Point out each leukocyte.
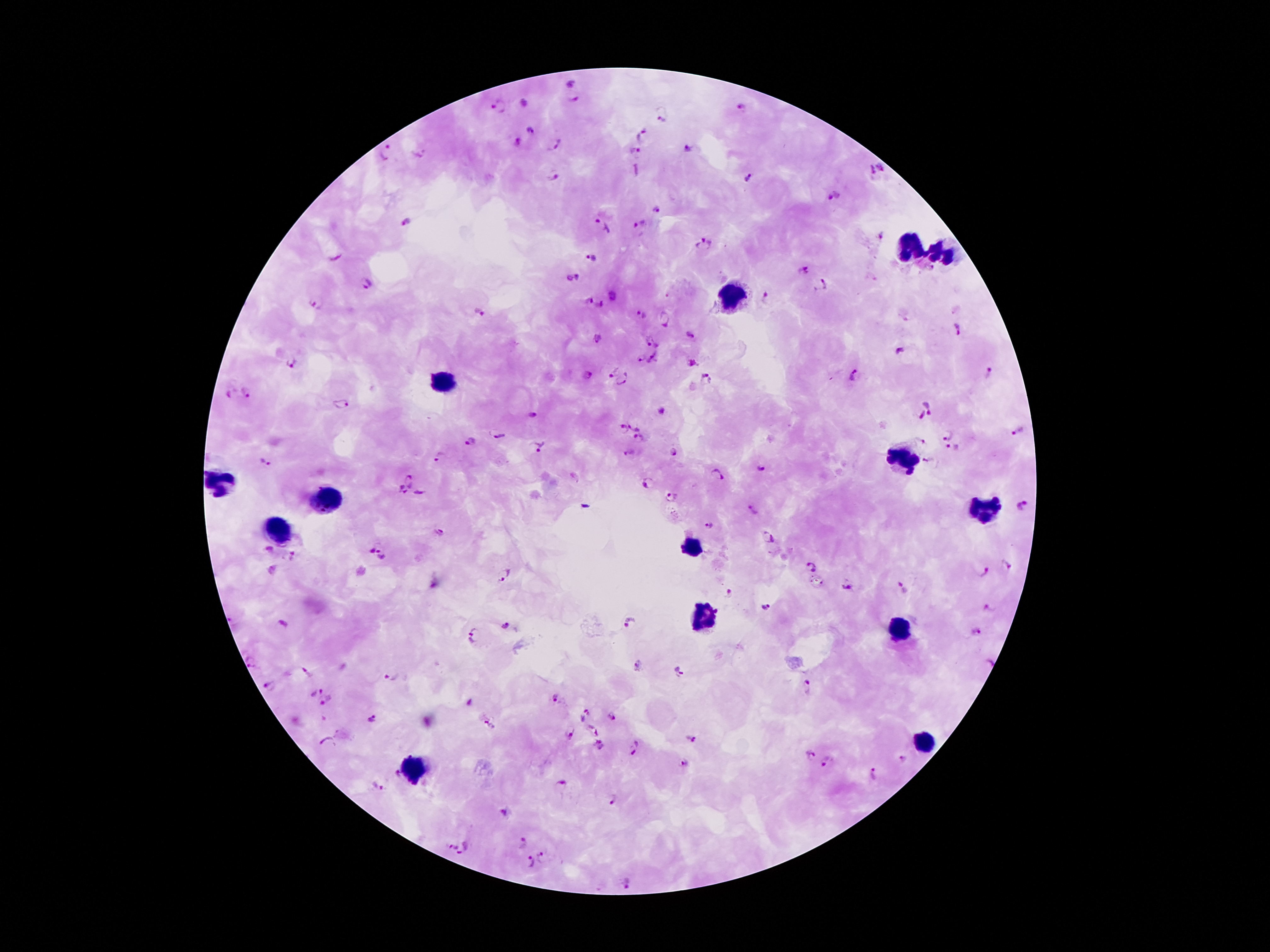

Approximate object centers, in pixels from the top-left corner.
Leukocytes: (x=910, y=247), (x=945, y=251), (x=734, y=296), (x=441, y=381), (x=901, y=459), (x=218, y=481), (x=326, y=500), (x=986, y=509), (x=277, y=534), (x=693, y=547), (x=704, y=618), (x=899, y=629), (x=923, y=741), (x=413, y=768).

Summary:
  - Malaria parasite locations: (x=573, y=84), (x=525, y=101), (x=574, y=102), (x=501, y=105), (x=743, y=105), (x=662, y=117), (x=528, y=128), (x=642, y=134), (x=520, y=142), (x=553, y=147), (x=385, y=150), (x=690, y=150), (x=634, y=153), (x=419, y=155), (x=883, y=166), (x=871, y=171), (x=553, y=175), (x=752, y=176), (x=834, y=199), (x=656, y=209), (x=407, y=221), (x=641, y=226), (x=602, y=229), (x=881, y=236), (x=703, y=246), (x=336, y=256), (x=591, y=259), (x=803, y=270), (x=571, y=277), (x=366, y=284), (x=821, y=286), (x=611, y=296), (x=766, y=300), (x=588, y=301), (x=314, y=303), (x=600, y=307), (x=640, y=314), (x=477, y=315), (x=664, y=319), (x=959, y=329), (x=690, y=333), (x=652, y=340), (x=597, y=341), (x=899, y=351), (x=640, y=357), (x=654, y=361), (x=290, y=362), (x=691, y=362), (x=612, y=369), (x=989, y=373), (x=588, y=374), (x=855, y=377), (x=705, y=380), (x=622, y=381), (x=248, y=392), (x=229, y=394), (x=341, y=404), (x=931, y=404), (x=533, y=413), (x=922, y=417), (x=633, y=423), (x=621, y=430), (x=1019, y=431), (x=948, y=433), (x=498, y=434), (x=638, y=438), (x=470, y=441), (x=924, y=443), (x=537, y=444), (x=953, y=449), (x=674, y=453), (x=631, y=454), (x=439, y=456), (x=264, y=461), (x=933, y=464), (x=761, y=469), (x=718, y=475), (x=412, y=479), (x=647, y=485), (x=400, y=492), (x=421, y=493), (x=671, y=498), (x=1025, y=505), (x=751, y=511), (x=708, y=524), (x=437, y=532), (x=767, y=537), (x=268, y=549), (x=369, y=549), (x=384, y=554), (x=294, y=557), (x=1008, y=566), (x=809, y=567), (x=983, y=572), (x=507, y=574), (x=848, y=586), (x=902, y=588), (x=729, y=594), (x=765, y=606), (x=989, y=607), (x=630, y=623), (x=503, y=628), (x=975, y=632), (x=475, y=637), (x=989, y=662), (x=255, y=663), (x=638, y=665), (x=679, y=671), (x=303, y=672), (x=391, y=678), (x=267, y=686), (x=808, y=686), (x=316, y=691), (x=554, y=698), (x=328, y=700), (x=586, y=714), (x=613, y=717), (x=371, y=721), (x=489, y=725), (x=570, y=732), (x=590, y=733), (x=692, y=739), (x=329, y=743), (x=599, y=748), (x=635, y=748), (x=808, y=755), (x=902, y=761), (x=828, y=764), (x=686, y=766), (x=397, y=774), (x=872, y=774), (x=561, y=783), (x=376, y=787), (x=613, y=798), (x=505, y=815), (x=522, y=845), (x=450, y=846), (x=466, y=851), (x=544, y=857), (x=525, y=862), (x=630, y=883)
  - Field of view: single
  - Stain: Giemsa
  - Image size: 1270×952 pixels
  - Magnification: 100x
  - Patient malaria status: positive for Plasmodium falciparum
  - Preparation: thick peripheral-blood smear
  - Capture: smartphone camera through the microscope eyepiece